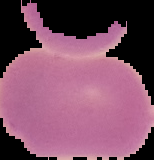
Summary:
  - Image type: cell region segmented out of the field of view; surrounding area masked to black
  - Result: no Plasmodium parasites seen
  - Preparation: thin blood film
  - Image size: 154×160 pixels